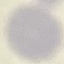 Result: no malaria parasites detected. Thin blood smear. Automatically extracted cell patch, resized to 64 × 64 pixels. Giemsa stain. Photographed with a smartphone camera at the microscope eyepiece.